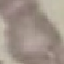

{
  "malaria_status": "uninfected",
  "stain": "Giemsa",
  "image_type": "cell patch, automatically extracted from a larger field of view and resized to 64 × 64 pixels",
  "preparation": "thin blood film",
  "capture": "smartphone camera at the microscope eyepiece"
}